Describe the morphology of the erythrocytes.
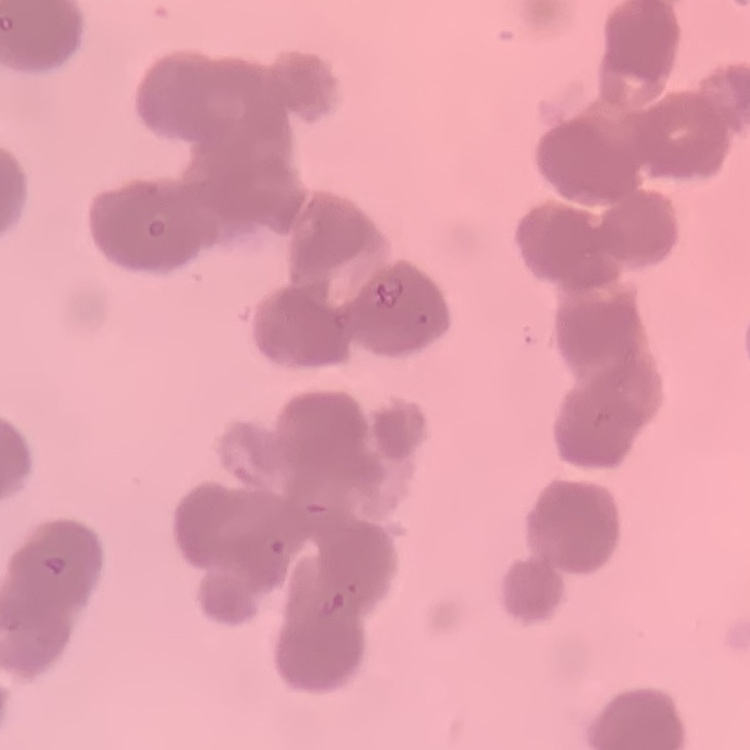

Rouleaux formation.

Summary:
  - Image type: square crop of a larger photomicrograph
  - Preparation: thin peripheral smear
  - Stain: Field's or Giemsa